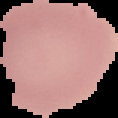

Summary:
  - Result: no malaria parasites seen
  - Image size: 118×118 pixels
  - Preparation: thin blood film
  - Image type: segmented cell region with the area outside set to black